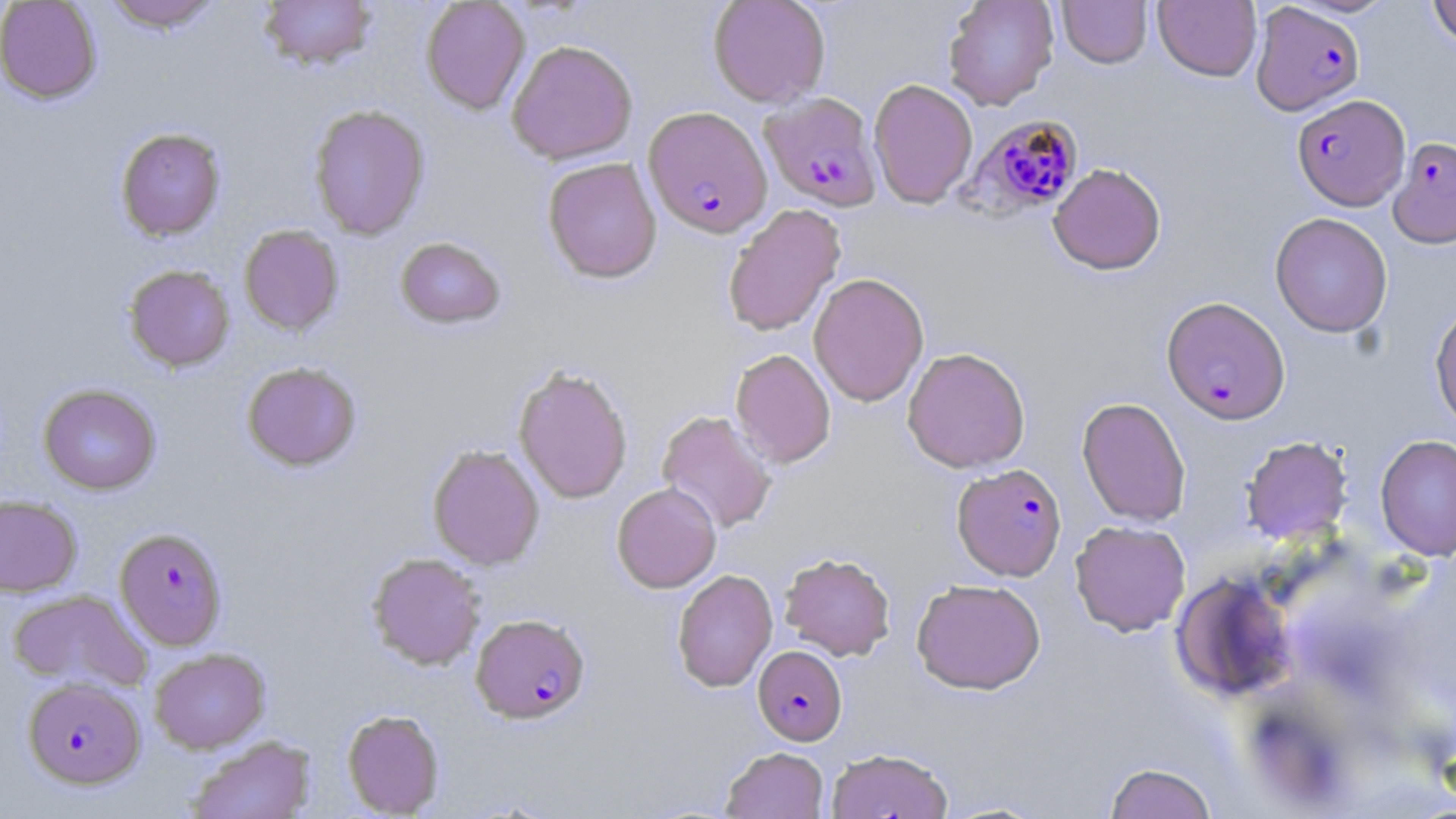

Summary:
  - Coordinate format: approximate bounding boxes as (x1,y1)-(x2,y2) corner pairs in pixels
  - Uninfected red blood cell locations: (1,0)-(102,104), (101,0)-(224,33), (256,0)-(379,72), (421,0)-(530,114), (707,0)-(831,108), (942,0)-(1059,111), (1056,0)-(1152,68), (1153,0)-(1261,82), (1428,0)-(1456,49), (506,39)-(638,165), (868,78)-(978,209), (308,104)-(430,240), (115,127)-(226,241), (542,157)-(662,284), (1048,163)-(1166,275), (723,204)-(845,336), (1270,212)-(1393,337), (239,224)-(344,336), (395,236)-(507,330), (123,264)-(235,372), (808,272)-(929,407), (1430,301)-(1456,432), (903,347)-(1030,473), (730,349)-(836,467), (241,361)-(362,472), (513,365)-(633,504), (38,383)-(161,495), (1077,397)-(1191,526), (657,410)-(777,534), (1375,434)-(1456,560), (1241,435)-(1353,544), (427,444)-(545,570), (612,482)-(721,593), (0,494)-(82,597), (1070,520)-(1191,636), (779,552)-(896,661), (366,553)-(486,670), (672,569)-(777,692), (1170,572)-(1296,702), (911,578)-(1046,694), (8,590)-(151,691), (150,648)-(270,754), (342,709)-(444,817), (184,735)-(317,819), (720,746)-(829,819), (827,748)-(952,819), (1104,762)-(1217,819)
  - Plasmodium falciparum-infected red blood cell locations: (1250,2)-(1365,115), (759,93)-(881,212), (1293,93)-(1410,210), (643,106)-(772,238), (966,113)-(1085,218), (1388,135)-(1456,249), (1161,296)-(1290,425), (952,463)-(1067,581), (115,526)-(228,650), (471,613)-(590,723), (752,645)-(846,745), (23,677)-(146,789)
  - Slide-level diagnosis: Plasmodium falciparum
  - Image size: 1456×819 pixels
  - Stain: May-Grünwald-Giemsa
  - Field of view: one of a larger specimen
  - Preparation: thin blood smear
  - Magnification: 1000x
  - Modality: light microscopy